Classify this cell by malaria status.
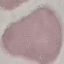
It is uninfected.

Summary:
  - Capture: smartphone through the microscope eyepiece
  - Preparation: thin blood smear
  - Image type: automatically extracted cell patch, resized to 64 × 64 pixels
  - Stain: Giemsa